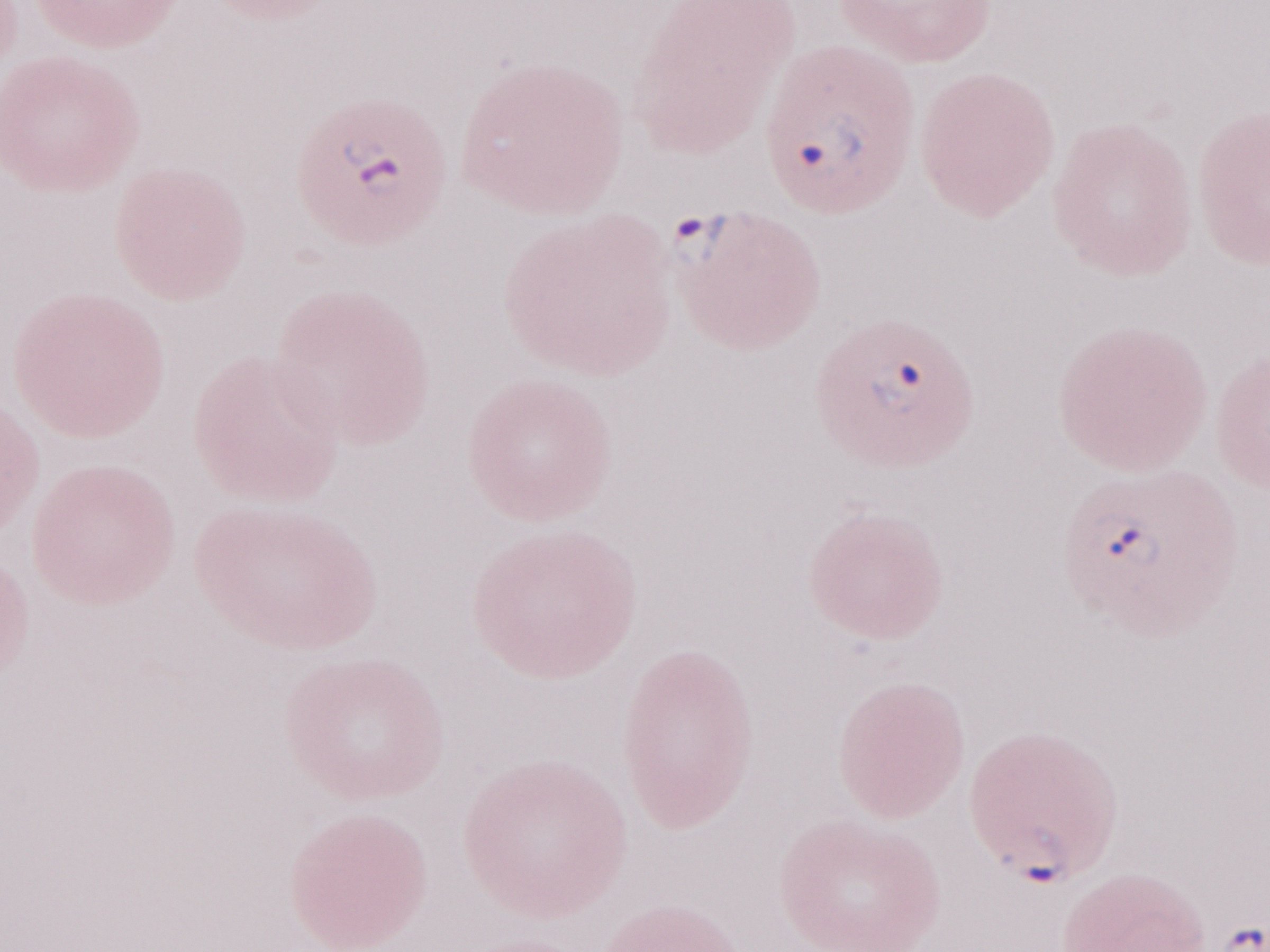 May-Grünwald-Giemsa-stained preparation. Thin blood film. 1,000x magnification. Malaria diagnosis (patient-level): positive. One field of this slide. Image is 1270×952 pixels. Olympus BX43 microscope and DP73 digital camera.